Give the location of every white blood cell.
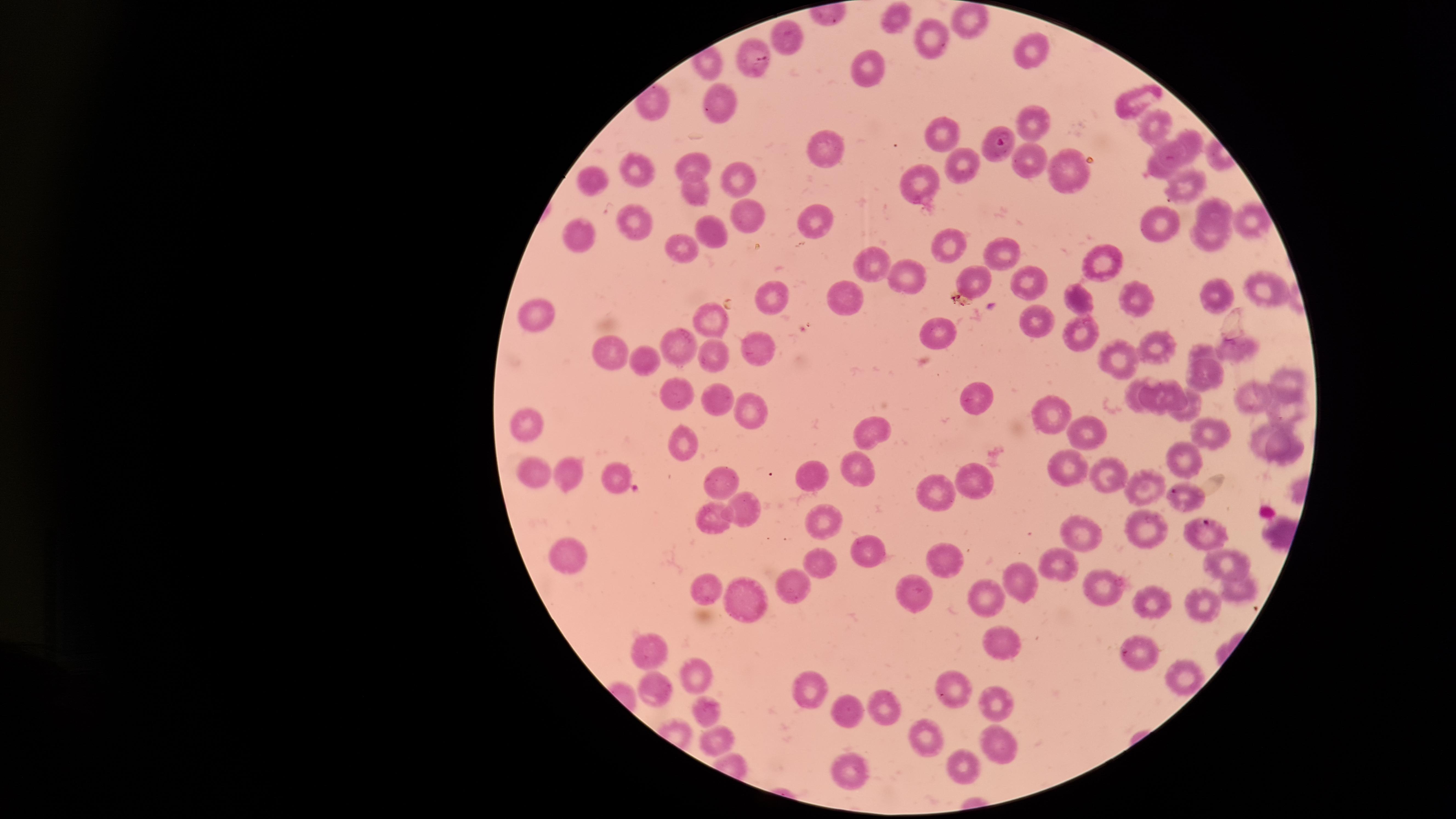
No white blood cells identified.

capture = smartphone photograph through the microscope eyepiece
parasitized red blood cells = approximate marker points as {x, y} in pixels: {754, 62}, {1003, 145}
presence = malaria parasites detected
visible region = circular
stain = Giemsa
field of view = single
preparation = thin smear of blood
uninfected red blood cells = approximate marker points as {x, y} in pixels: {969, 17}, {896, 18}, {787, 36}, {930, 37}, {1037, 50}, {870, 71}, {721, 100}, {1132, 101}, {1029, 119}, {1151, 124}, {944, 133}, {1191, 142}, {822, 148}, {1175, 155}, {696, 157}, {1027, 160}, {961, 164}, {643, 169}, {1066, 169}, {1159, 171}, {586, 174}, {736, 178}, {1188, 183}, {923, 185}, {696, 186}, {1215, 209}, {748, 214}, {635, 219}, {1248, 220}, {1155, 224}, {811, 227}, {579, 230}, {711, 231}, {1209, 242}, {685, 248}, {949, 248}, {998, 251}, {874, 260}, {1099, 260}, {904, 274}, {1023, 277}, {975, 280}, {1265, 290}, {778, 292}, {1220, 294}, {1078, 297}, {842, 298}, {1138, 298}, {533, 314}, {714, 315}, {1031, 321}, {1079, 330}, {944, 331}, {681, 342}, {756, 345}, {1158, 347}, {1202, 348}, {1240, 348}, {616, 354}, {719, 356}, {643, 357}, {1123, 358}, {1203, 376}, {1284, 381}, {1133, 393}, {673, 394}, {974, 395}, {1175, 395}, {1153, 398}, {1257, 398}, {720, 400}, {751, 411}, {1051, 412}, {1193, 412}, {1287, 413}, {530, 424}, {1085, 431}, {1211, 431}, {875, 432}, {684, 440}, {1261, 440}, {1288, 451}, {1182, 453}, {856, 461}, {1066, 465}, {572, 469}, {615, 471}, {530, 472}, {811, 472}, {1104, 477}, {970, 478}, {718, 483}, {1150, 483}, {939, 484}, {743, 510}, {823, 517}, {712, 522}, {1142, 523}, {1085, 533}, {875, 548}, {944, 552}, {570, 555}, {1225, 558}, {829, 561}, {1060, 562}, {1017, 578}, {793, 584}, {1100, 584}, {709, 585}, {914, 587}, {1236, 588}, {986, 593}, {741, 600}, {1154, 603}, {1204, 606}, {1003, 641}, {656, 648}, {1138, 648}, {696, 671}, {1180, 674}, {656, 686}, {811, 686}, {950, 686}, {994, 703}, {882, 704}, {844, 708}, {711, 709}, {920, 730}, {999, 738}, {718, 739}, {960, 764}, {851, 767}
species = Plasmodium falciparum
image size = 1456×819 pixels